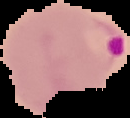
image type = segmented cell region on a black background
image size = 130×118 pixels
result = Plasmodium parasites detected
preparation = thin blood smear